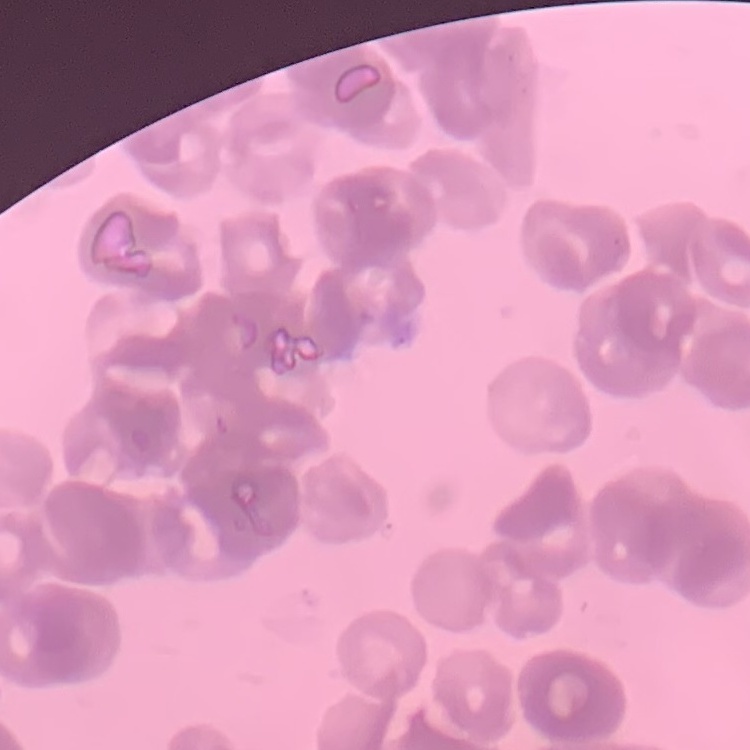
Summary:
  - Red blood cell morphology: rouleaux formation
  - Stain: Field's or Giemsa
  - Image type: square crop of a larger photomicrograph
  - Preparation: thin peripheral smear